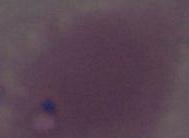 Captured at 1000x magnification. Photomicrograph. A red blood cell is shown.